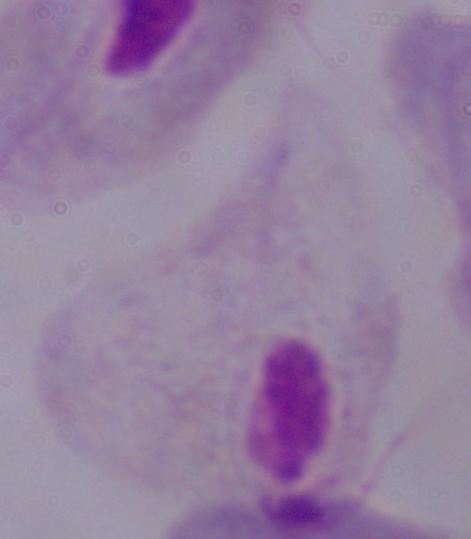

Summary:
  - Identification: trichomonad
  - Modality: photomicrograph
  - Magnification: 1000x